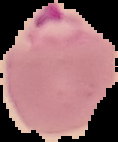
Summary:
  - Image type: segmented cell region on a black background
  - Malaria status: parasitized
  - Image size: 118×142 pixels
  - Preparation: thin blood film